Report the malaria status of this cell.
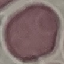
It is uninfected.

Giemsa stain. Photographed with a smartphone camera at the microscope eyepiece. Thin blood film. Cell patch, automatically extracted from a larger field of view and resized to 64 × 64 pixels.